Name the cell type shown.
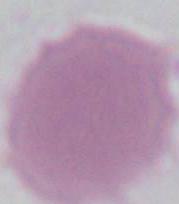

An erythrocyte.

Summary:
  - Modality: photomicrograph
  - Magnification: 1000x